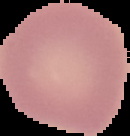

Summary:
  - Image size: 130×136 pixels
  - Image type: segmented cell region on a black background
  - Preparation: thin blood film
  - Result: negative for Plasmodium parasites